Describe the morphology of the erythrocytes.
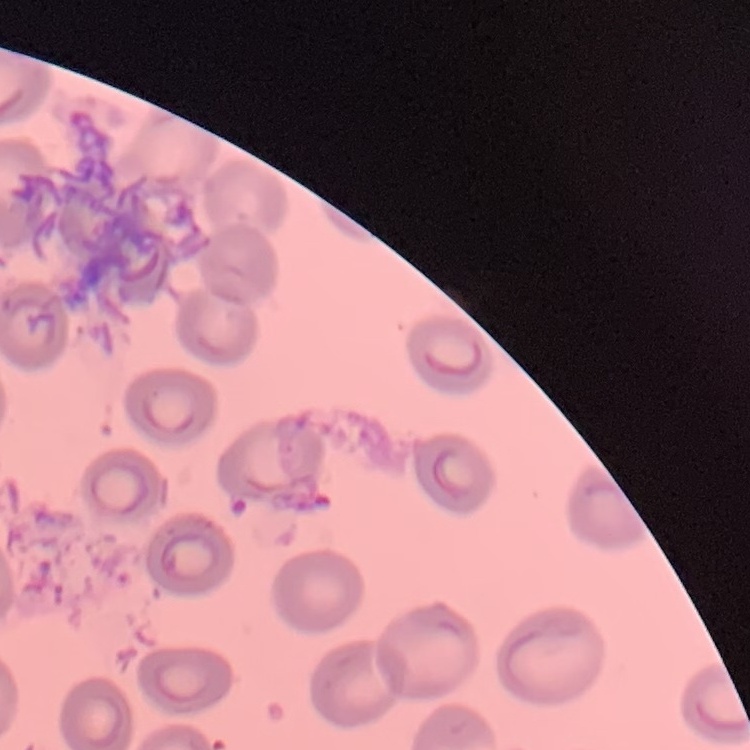
No rouleaux formation.

Thin blood smear. Stained with either Field's or Giemsa. Square crop of a larger photomicrograph.